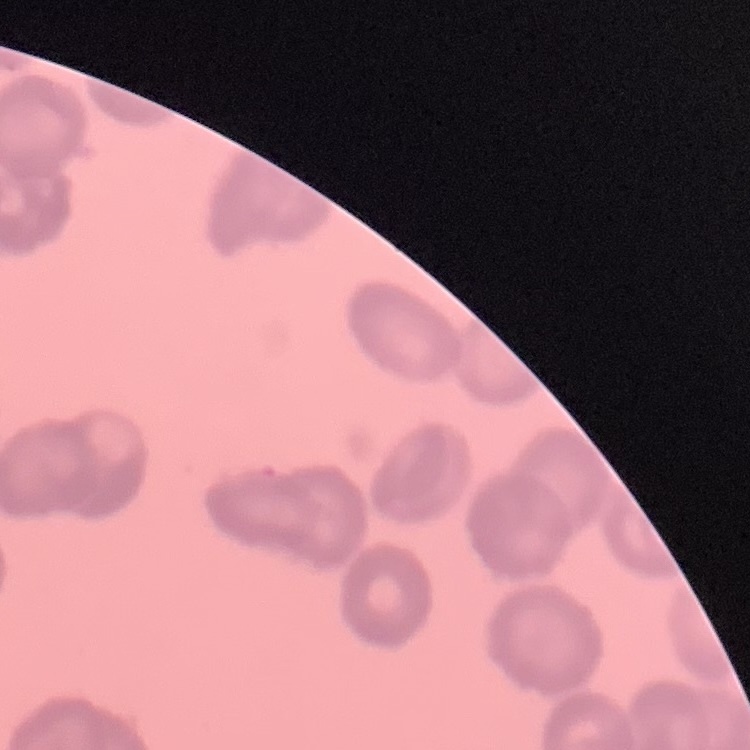
red blood cell morphology = rouleaux formation
image type = square crop of a larger photomicrograph
stain = Field's or Giemsa
preparation = thin blood smear